Assess this cell for malaria.
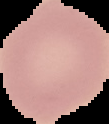

It is uninfected.

image type = segmented cell region with the area outside set to black
image size = 109×124 pixels
preparation = thin blood smear